Locate the red blood cells and classify each one as P. falciparum-infected, uninfected, or of indeterminate infection status.
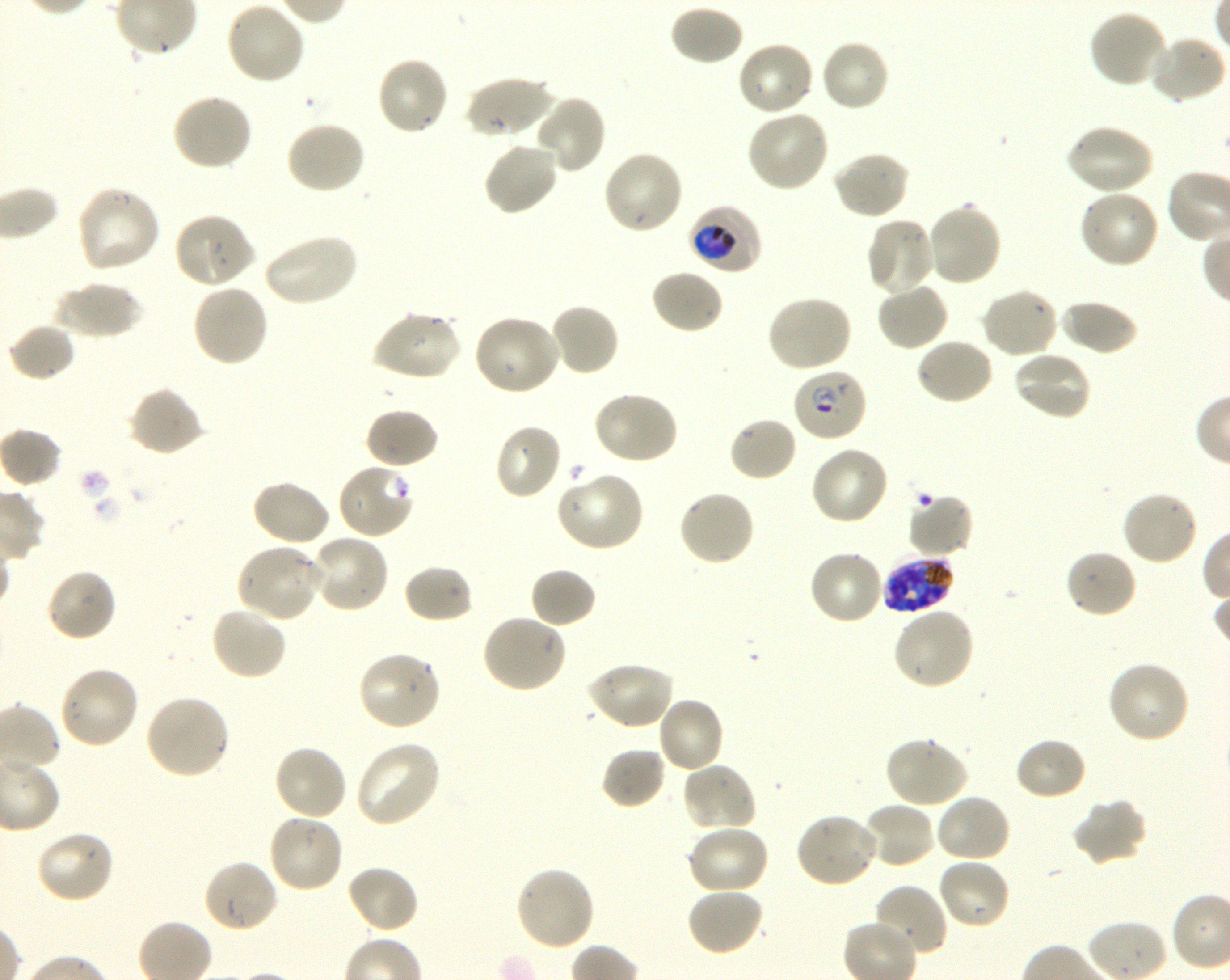

Approximate bounding boxes as {x1, y1, x2, y2} in pixels. Not every red blood cell is marked. A life-cycle stage — or a range of stages, where the recorded stages span more than one — follows each staged infected red blood cell.
Infected red blood cells: {688, 205, 763, 275} trophozoite; {791, 368, 867, 443} early ring to early trophozoite; {881, 556, 955, 614} schizont; {202, 858, 279, 934}.
Red blood cells of indeterminate infection status: {337, 463, 415, 541}, {906, 493, 975, 559}.
Uninfected red blood cells: {225, 1, 306, 85}, {669, 4, 745, 67}, {1088, 8, 1167, 89}, {1145, 35, 1226, 104}, {820, 38, 891, 113}, {737, 40, 816, 117}, {375, 55, 451, 137}, {463, 75, 553, 140}, {170, 93, 254, 172}, {534, 94, 607, 174}, {745, 110, 830, 193}, {285, 120, 367, 196}, {1065, 123, 1154, 196}, {482, 140, 560, 217}, {601, 149, 684, 236}, {831, 151, 910, 220}, {75, 186, 162, 275}, {1077, 190, 1161, 270}, {926, 203, 1003, 287}, {173, 211, 257, 288}, {864, 217, 935, 297}, {263, 232, 359, 308}, {650, 268, 725, 334}, {53, 280, 142, 340}, {876, 282, 948, 352}, {191, 283, 270, 368}, {980, 287, 1060, 359}, {764, 295, 853, 373}, {1059, 299, 1139, 356}, {549, 302, 620, 377}, {371, 309, 462, 382}, {472, 313, 563, 397}, {8, 322, 77, 382}, {915, 337, 995, 406}, {1010, 350, 1092, 422}, {128, 386, 204, 456}, {592, 389, 679, 465}, {364, 407, 439, 470}, {728, 416, 798, 483}, {493, 422, 563, 501}, {4, 430, 59, 487}, {809, 444, 889, 526}, {556, 471, 645, 552}, {249, 479, 332, 547}, {678, 489, 756, 568}, {1120, 490, 1201, 567}, {309, 532, 392, 613}, {236, 542, 324, 623}, {807, 548, 885, 626}, {1064, 548, 1138, 619}, {402, 563, 474, 624}, {529, 566, 597, 629}, {44, 567, 118, 643}, {210, 605, 289, 681}, {892, 607, 976, 691}, {480, 613, 568, 693}, {357, 650, 443, 731}, {1106, 659, 1191, 745}, {586, 660, 674, 730}, {58, 665, 140, 750}, {144, 693, 231, 780}, {656, 697, 726, 774}, {884, 736, 968, 809}, {1014, 737, 1088, 802}, {354, 740, 442, 828}, {273, 743, 348, 822}, {601, 748, 666, 810}, {680, 761, 758, 834}, {934, 793, 1012, 863}, {1071, 798, 1148, 867}, {863, 801, 937, 870}, {793, 811, 880, 889}, {267, 813, 345, 894}, {685, 824, 771, 896}, {34, 830, 115, 904}, {937, 858, 1011, 931}, {346, 863, 420, 934}, {513, 865, 595, 951}, {873, 883, 947, 959}, {685, 887, 766, 959}.

{
  "objective": "100x, oil immersion, numerical aperture 1.30",
  "life_cycle_stages_observed": "trophozoite, schizont",
  "preparation": "thin blood film",
  "field_of_view": "single",
  "image_size": "1230×980 pixels",
  "stain": "Giemsa",
  "donor_blood_group": "O+",
  "culture": "in-vitro P. falciparum strain 3D7, shaking"
}